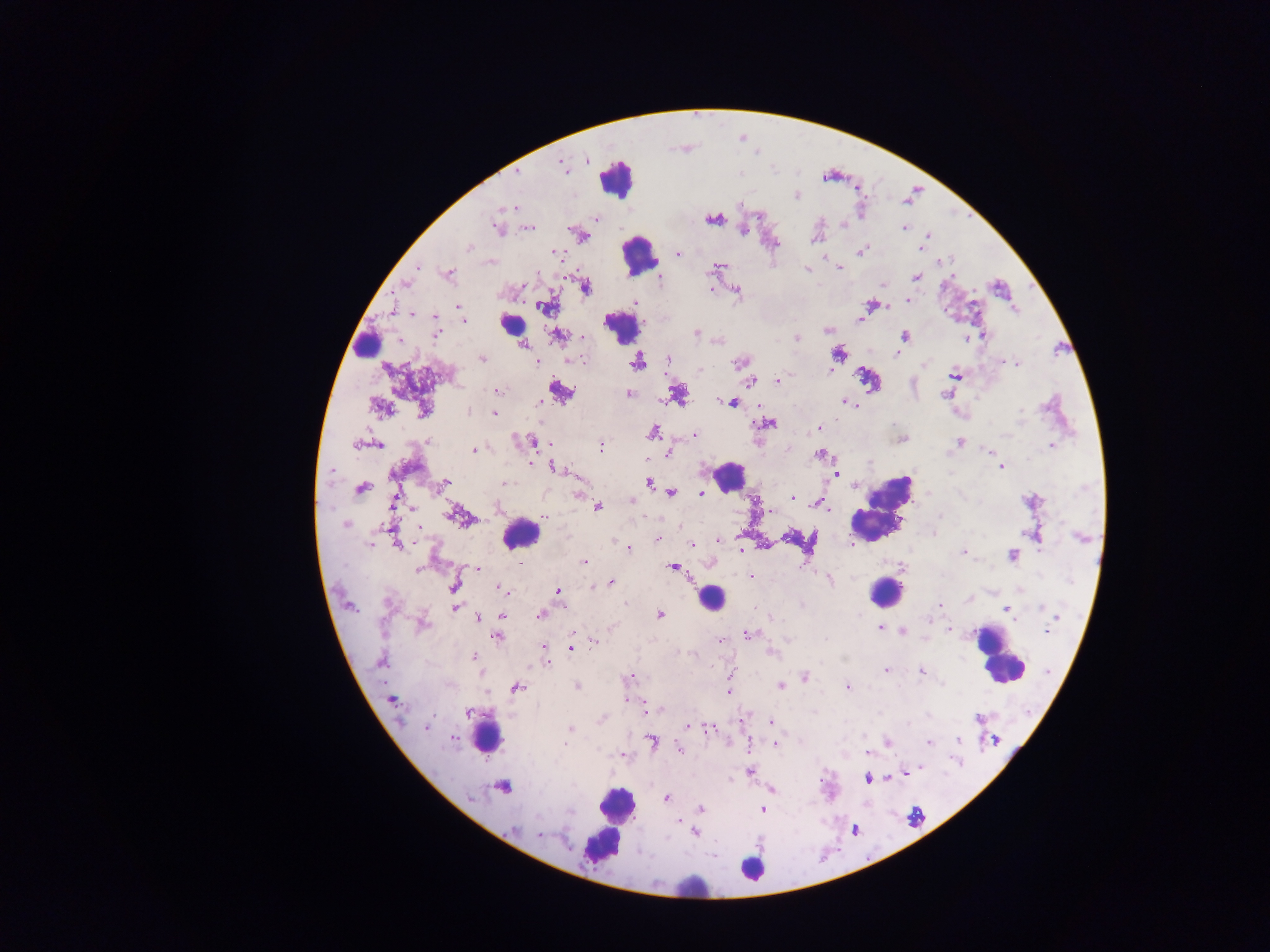
Approximate centers as x y in pixels. Plasmodium parasite locations: 562 166; 517 172; 796 195; 513 207; 595 218; 711 220; 497 226; 904 227; 529 228; 743 230; 927 237; 774 245; 468 247; 921 249; 861 252; 554 253; 678 254; 941 263; 720 266; 417 267; 839 267; 806 269; 414 270; 449 273; 538 273; 916 277; 660 280; 406 284; 882 285; 586 287; 710 289; 737 291; 908 300; 635 303; 886 306; 459 307; 545 308; 413 315; 435 317; 860 319; 463 325; 827 331; 696 333; 436 335; 984 335; 904 336; 557 337; 581 337; 796 338; 966 339; 400 340; 839 353; 897 354; 481 358; 668 358; 571 360; 579 360; 537 361; 637 361; 1004 361; 739 363; 1011 363; 1017 364; 924 365; 700 370; 829 371; 953 375; 777 380; 750 382; 497 390; 561 392; 678 394; 629 395; 946 395; 540 402; 731 402; 846 403; 853 404; 381 408; 424 408; 1020 411; 468 412; 494 413; 767 423; 819 428; 652 432; 695 435; 903 440; 533 442; 959 442; 543 443; 356 444; 378 445; 601 446; 1051 446; 474 450; 989 450; 669 452; 819 454; 530 462; 1002 467; 554 468; 331 470; 837 473; 392 475; 649 482; 444 483; 505 483; 440 486; 361 489; 671 492; 701 494; 579 495; 792 498; 631 500; 393 502; 818 505; 598 507; 827 509; 772 511; 545 516; 940 516; 459 517; 345 525; 419 528; 935 532; 657 539; 718 539; 397 543; 691 544; 370 545; 629 548; 741 551; 964 554; 1013 555; 585 562; 672 567; 478 568; 417 570; 751 576; 829 580; 611 583; 454 586; 500 588; 558 592; 625 603; 939 604; 350 607; 456 607; 1041 607; 1005 609; 660 614; 540 615; 502 616; 1057 616; 478 618; 771 618; 422 624; 879 627; 949 630; 902 632; 1046 632; 747 635; 496 636; 720 640; 594 643; 571 647; 545 648; 771 652; 473 656; 380 661; 547 662; 886 670; 922 671; 631 676; 805 676; 577 686; 781 686; 517 687; 848 687; 728 693; 391 700; 627 700; 646 709; 468 713; 978 718; 601 720; 772 722; 909 723; 426 727; 688 728; 569 729; 709 729; 453 738; 651 740; 958 740; 994 740; 888 742; 566 743; 929 743; 775 744; 680 749; 867 753; 622 755; 919 767; 750 771; 908 772; 868 779; 504 786; 773 790; 472 798; 666 798; 702 809; 762 810; 570 812; 678 822; 684 829; 514 830; 695 832; 539 834. Leukocyte locations: 616 179; 638 255; 515 323; 620 324; 362 343; 727 474; 881 509; 520 535; 886 592; 710 598; 997 656; 489 738; 615 807; 606 832; 752 868; 690 884. Sample from Ghana. Mobile-phone photograph taken through the microscope. Thick blood film. Image is 1270×952 pixels. Single field of view.